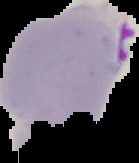
Summary:
  - Image type: segmented cell region with the area outside set to black
  - Image size: 139×163 pixels
  - Preparation: thin blood film
  - Malaria status: parasitized